Classify this cell by malaria status.
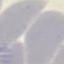
Uninfected.

Summary:
  - Image type: cell patch, automatically extracted from a larger field of view and resized to 64 × 64 pixels
  - Stain: Giemsa
  - Capture: smartphone through the microscope eyepiece
  - Preparation: thin blood smear